Name the parasite shown.
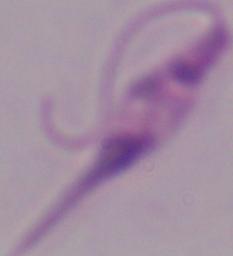

Leishmania.

modality = micrograph
magnification = 1000x